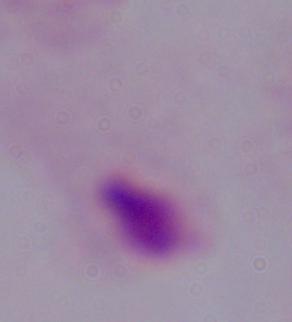

{
  "magnification": "1000x",
  "modality": "photomicrograph",
  "identification": "trichomonad"
}